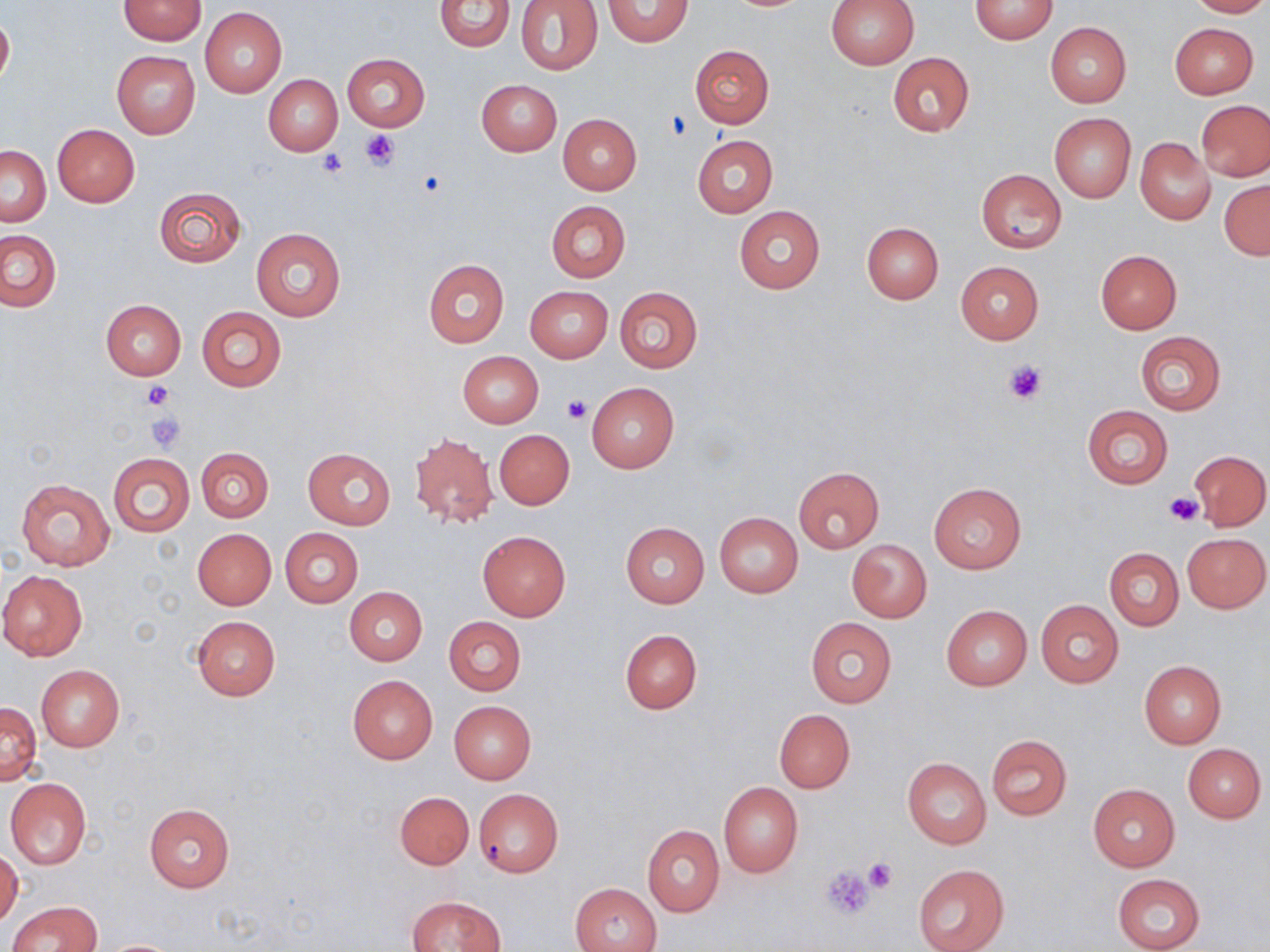

slide-level diagnosis = negative for blood parasites
modality = light microscopy
field of view = one of a larger specimen
platelet locations = approximate bounding boxes as (x1,y1)-(x2,y2) corner pairs in pixels: (667,110)-(692,140), (360,128)-(401,171), (316,149)-(349,178), (1003,359)-(1047,406), (141,379)-(173,409), (562,394)-(589,423), (145,413)-(185,452), (1166,492)-(1204,526), (863,857)-(897,893), (821,865)-(876,919)
image size = 1270×952 pixels
magnification = 1000x
preparation = thin blood smear
uninfected red blood cell locations = approximate bounding boxes as (x1,y1)-(x2,y2) corner pairs in pixels: (118,0)-(207,45), (433,0)-(515,51), (517,0)-(603,75), (602,0)-(693,47), (827,0)-(920,68), (970,0)-(1057,44), (1187,0)-(1270,18), (199,7)-(286,97), (0,11)-(14,90), (1045,22)-(1131,108), (1170,22)-(1258,98), (689,44)-(775,128), (112,50)-(200,138), (888,52)-(975,136), (342,53)-(429,131), (264,75)-(343,156), (477,79)-(562,156), (1197,100)-(1270,181), (557,114)-(641,195), (1049,114)-(1136,202), (53,123)-(140,207), (692,135)-(777,217), (1135,137)-(1215,225), (1,145)-(50,225), (976,169)-(1066,253), (1219,179)-(1270,260), (154,186)-(246,268), (546,201)-(630,282), (734,205)-(825,294), (860,222)-(943,304), (250,228)-(346,322), (1,230)-(60,312), (1095,249)-(1182,333), (423,258)-(509,348), (955,261)-(1044,344), (526,285)-(613,362), (615,287)-(702,372), (100,300)-(186,380), (196,307)-(286,390), (1134,331)-(1226,415), (458,351)-(543,427), (587,382)-(679,473), (1082,405)-(1173,487), (495,429)-(574,509), (409,431)-(498,527), (196,447)-(273,521), (303,447)-(395,529), (1189,450)-(1269,530), (108,453)-(195,537), (794,466)-(884,552), (15,477)-(114,571), (929,482)-(1025,573), (716,513)-(803,598), (620,522)-(710,608), (279,527)-(363,607), (192,529)-(276,609), (478,531)-(570,622), (1183,532)-(1269,612), (846,539)-(932,623), (1105,547)-(1183,630), (0,570)-(88,660), (344,587)-(427,665), (1036,599)-(1124,688), (942,605)-(1031,690), (191,615)-(280,701), (444,617)-(525,695), (806,617)-(898,707), (620,629)-(702,714), (1139,660)-(1226,748), (36,664)-(125,750), (347,674)-(437,763), (448,700)-(537,783), (0,702)-(42,783), (773,709)-(855,793), (986,734)-(1072,820), (1183,743)-(1266,822), (902,756)-(991,849), (5,779)-(91,869), (718,780)-(803,878), (1087,784)-(1179,872), (473,786)-(564,878), (393,791)-(473,869), (143,804)-(236,892), (642,825)-(724,916), (0,848)-(23,927), (912,863)-(1010,952), (1112,873)-(1205,952), (570,883)-(662,952), (408,895)-(504,951), (8,901)-(102,952), (99,939)-(186,951)
stain = May-Grünwald-Giemsa